State the blood parasite species.
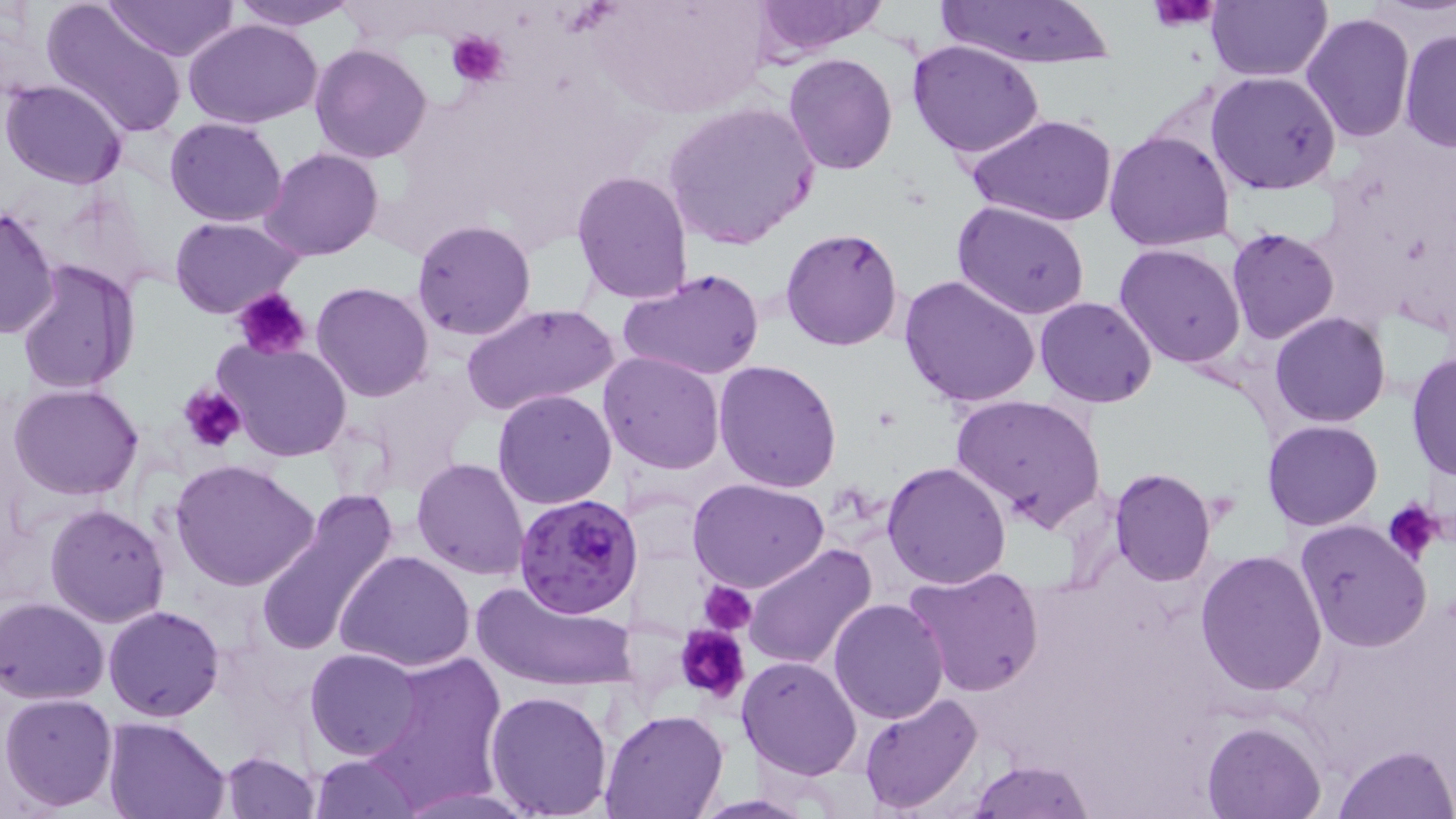
Plasmodium falciparum.

field of view = one of a larger specimen
Plasmodium falciparum-infected red blood cell locations = approximate bounding boxes as (x1,y1)-(x2,y2) corner pairs in pixels: (514,493)-(643,618)
uninfected red blood cell locations = approximate bounding boxes as (x1,y1)-(x2,y2) corner pairs in pixels: (41,0)-(189,140), (105,0)-(240,63), (232,0)-(361,29), (1206,0)-(1331,82), (935,2)-(1120,70), (748,3)-(886,59), (1300,12)-(1415,142), (184,20)-(323,130), (1399,28)-(1456,157), (906,37)-(1045,158), (309,44)-(433,164), (783,51)-(899,174), (1206,71)-(1340,195), (1,77)-(128,188), (663,101)-(820,248), (963,111)-(1120,228), (164,116)-(288,226), (1103,128)-(1235,252), (260,147)-(384,261), (570,168)-(694,306), (953,202)-(1092,319), (0,203)-(59,342), (169,214)-(305,318), (411,219)-(537,341), (781,227)-(904,351), (1226,228)-(1339,345), (1114,242)-(1246,368), (17,260)-(144,396), (618,269)-(766,384), (899,275)-(1041,410), (312,282)-(435,403), (1035,296)-(1156,407), (462,301)-(618,420), (1270,312)-(1392,427), (215,339)-(351,461), (598,352)-(726,475), (1407,352)-(1455,482), (714,359)-(843,492), (8,384)-(146,501), (493,390)-(617,509), (950,393)-(1105,531), (1263,419)-(1382,530), (412,457)-(529,580), (171,458)-(319,593), (881,460)-(1012,589), (1107,467)-(1215,586), (687,476)-(829,593), (254,488)-(401,659), (44,503)-(169,628), (1293,519)-(1434,651), (744,542)-(877,671), (1194,549)-(1329,695), (336,551)-(477,674), (901,566)-(1045,699), (470,576)-(639,693), (0,598)-(109,704), (827,598)-(949,723), (103,605)-(224,721), (306,646)-(423,761), (369,651)-(507,804), (738,656)-(862,779), (484,688)-(613,817), (1,692)-(119,810), (859,692)-(985,813), (599,708)-(728,818), (103,716)-(232,818), (1202,719)-(1325,818), (1334,743)-(1454,819), (218,751)-(320,819), (310,753)-(422,818), (967,759)-(1095,818)
preparation = thin blood smear
magnification = 1000x
platelet locations = approximate bounding boxes as (x1,y1)-(x2,y2) corner pairs in pixels: (1148,4)-(1219,30), (447,29)-(511,88), (232,287)-(314,362), (179,385)-(247,455), (1383,498)-(1444,566), (702,582)-(756,633), (676,623)-(751,702)
modality = light microscopy
image size = 1456×819 pixels
stain = May-Grünwald-Giemsa